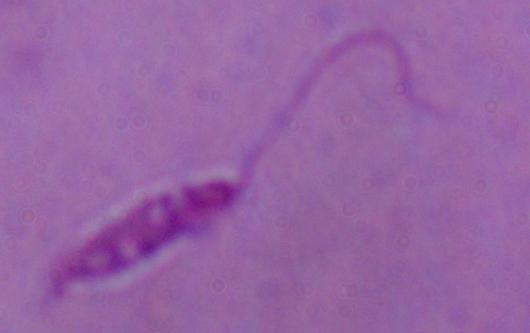
A Leishmania parasite is shown. Captured at 1000x magnification. Photomicrograph.